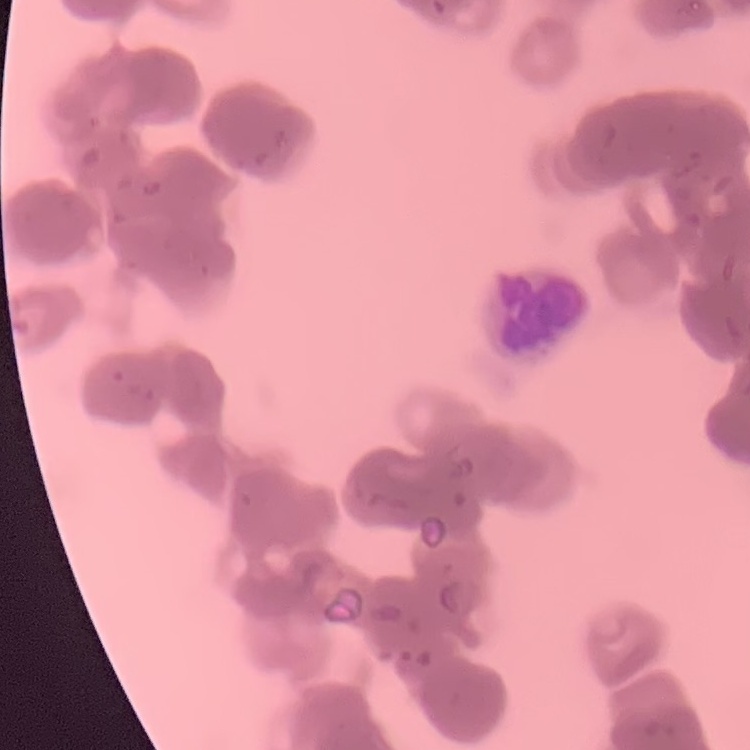

erythrocyte morphology = rouleaux formation
image type = one tile cut from a larger photomicrograph
preparation = thin blood smear
stain = Field's or Giemsa